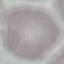

Summary:
  - Malaria status: uninfected
  - Capture: smartphone through the microscope eyepiece
  - Stain: Giemsa
  - Image type: cell patch, automatically extracted from a larger field of view and resized to 64 × 64 pixels
  - Preparation: thin blood smear